Assess this cell for malaria.
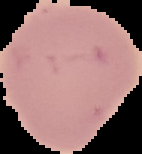
It is uninfected.

The area outside the segmented cell region is set to black. Image is 142×154 pixels. From a thin blood smear.